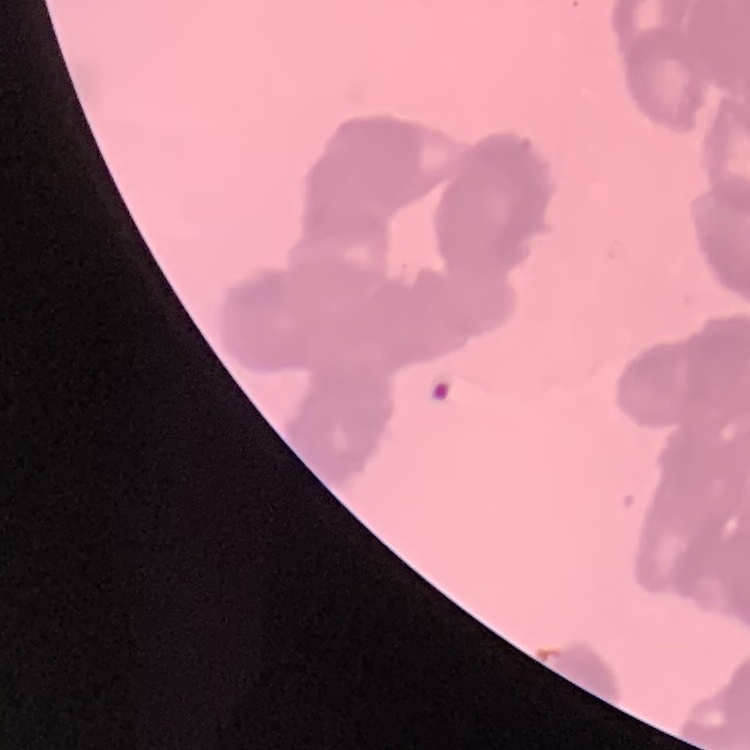
{
  "erythrocyte_morphology": "rouleaux formation",
  "image_type": "square crop of a larger photomicrograph",
  "stain": "Field's or Giemsa",
  "preparation": "thin blood smear"
}